Classify this cell by malaria status.
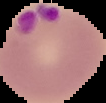
It is parasitized.

Summary:
  - Preparation: thin blood film
  - Image size: 106×103 pixels
  - Image type: segmented cell region on a black background